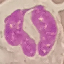
malaria status = uninfected
image type = cell patch, automatically extracted from a larger field of view and resized to 64 × 64 pixels
stain = Giemsa
capture = smartphone camera at the microscope eyepiece
preparation = thin blood film